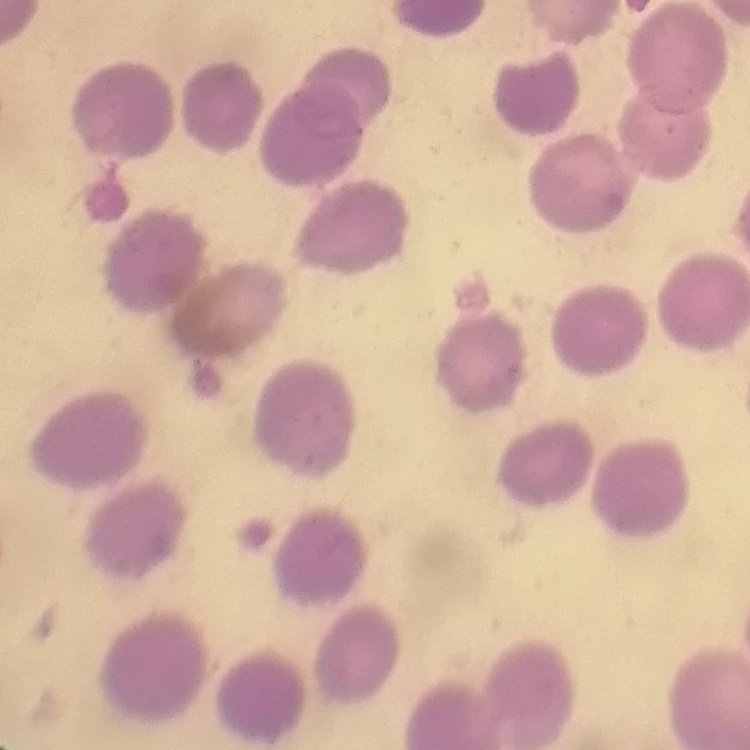 The erythrocytes exhibit no rouleaux formation. Stained with either Field's or Giemsa. Thin blood film. Square crop of a larger photomicrograph.